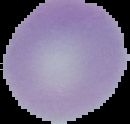

preparation = thin blood smear
image size = 130×124 pixels
malaria status = uninfected
image type = segmented cell region on a black background